Assess this cell for malaria.
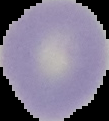
Uninfected.

image size = 109×121 pixels
preparation = thin blood film
image type = segmented cell region with the area outside set to black